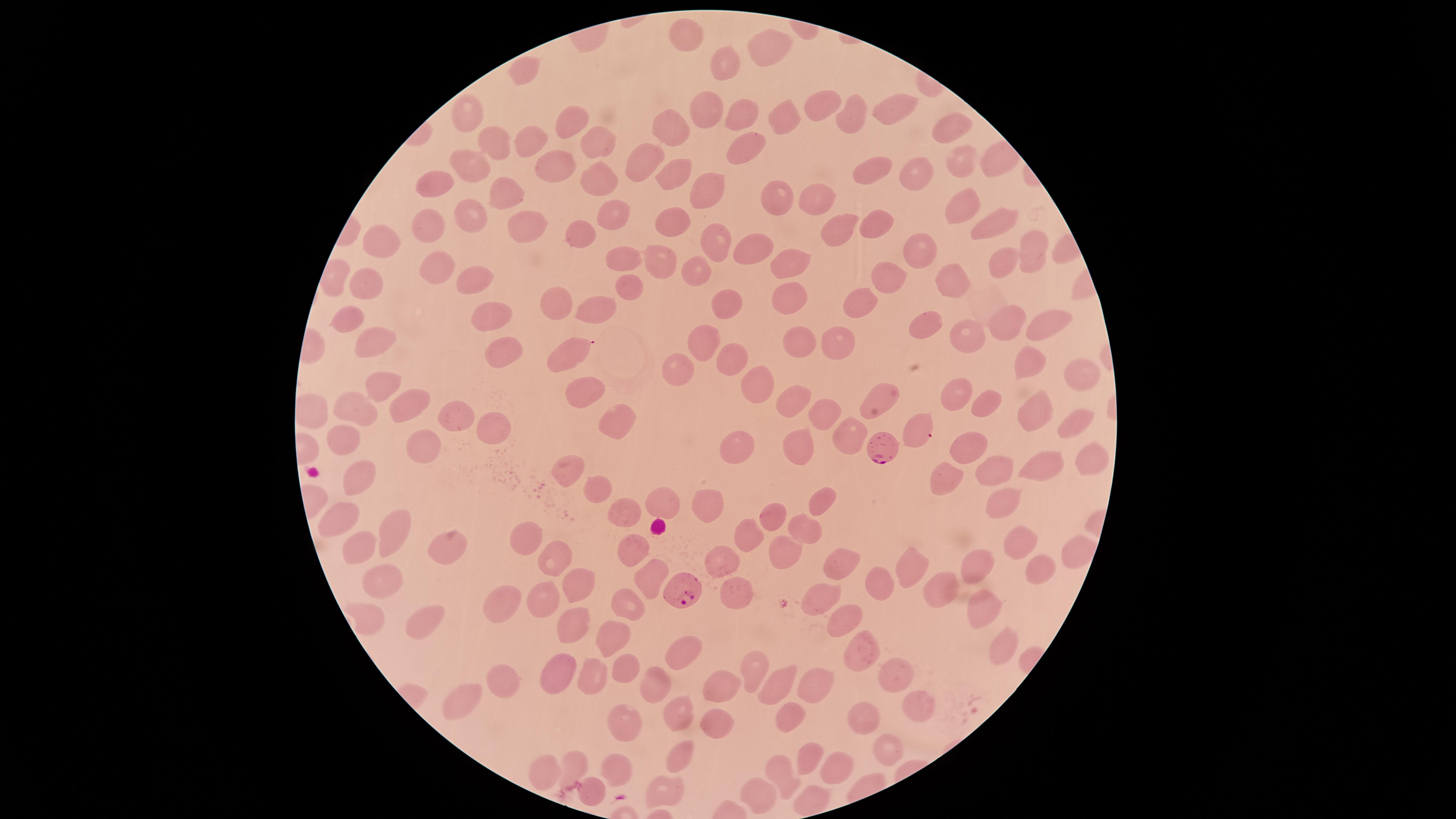
{
  "visible_region": "circular",
  "preparation": "thin blood film",
  "capture": "smartphone photograph through the microscope eyepiece",
  "parasitized_red_blood_cells": "approximate marker points, in pixels from the top-left corner: (x=876, y=453), (x=683, y=595)",
  "species": "Plasmodium falciparum",
  "field_of_view": "single",
  "image_size": "1456×819 pixels",
  "uninfected_red_blood_cells": "approximate marker points, in pixels from the top-left corner: (x=689, y=28), (x=774, y=44), (x=727, y=61), (x=521, y=67), (x=829, y=98), (x=475, y=105), (x=897, y=109), (x=707, y=114), (x=853, y=116), (x=739, y=117), (x=782, y=118), (x=572, y=122), (x=671, y=126), (x=950, y=130), (x=533, y=140), (x=592, y=144), (x=749, y=144), (x=495, y=146), (x=645, y=156), (x=994, y=157), (x=962, y=159), (x=473, y=161), (x=559, y=164), (x=676, y=168), (x=871, y=172), (x=919, y=173), (x=595, y=175), (x=439, y=185), (x=702, y=190), (x=504, y=194), (x=818, y=194), (x=778, y=199), (x=967, y=206), (x=468, y=214), (x=608, y=215), (x=678, y=218), (x=875, y=221), (x=993, y=223), (x=525, y=224), (x=426, y=225), (x=836, y=225), (x=578, y=233), (x=716, y=239), (x=753, y=244), (x=384, y=246), (x=922, y=251), (x=1030, y=252), (x=625, y=258), (x=791, y=258), (x=1001, y=259), (x=658, y=263), (x=698, y=270), (x=439, y=272), (x=889, y=275), (x=475, y=277), (x=955, y=277), (x=369, y=282), (x=632, y=285), (x=785, y=292), (x=555, y=298), (x=725, y=298), (x=599, y=302), (x=859, y=307), (x=494, y=309), (x=1048, y=317), (x=349, y=318), (x=922, y=325), (x=1005, y=325), (x=964, y=337), (x=712, y=338), (x=840, y=339), (x=373, y=342), (x=807, y=342), (x=506, y=347), (x=575, y=352), (x=725, y=354), (x=676, y=363), (x=1030, y=364), (x=1085, y=375), (x=384, y=382), (x=754, y=383), (x=578, y=386), (x=884, y=392), (x=960, y=396), (x=793, y=400), (x=349, y=402), (x=827, y=405), (x=988, y=405), (x=1041, y=405), (x=411, y=407), (x=452, y=411), (x=620, y=411), (x=491, y=422), (x=1074, y=422), (x=914, y=425), (x=855, y=426), (x=345, y=437), (x=799, y=442), (x=974, y=443), (x=736, y=444), (x=420, y=447), (x=1095, y=458), (x=1042, y=462), (x=997, y=466), (x=567, y=473), (x=944, y=474), (x=355, y=479), (x=596, y=496), (x=664, y=497), (x=1001, y=499), (x=821, y=501), (x=705, y=503), (x=630, y=509), (x=767, y=511), (x=335, y=516), (x=803, y=525), (x=395, y=537), (x=527, y=538), (x=1015, y=538), (x=748, y=539), (x=357, y=543), (x=447, y=543), (x=777, y=548), (x=631, y=549), (x=1074, y=552), (x=549, y=553), (x=835, y=560), (x=918, y=561), (x=723, y=563), (x=982, y=563), (x=1043, y=566), (x=646, y=574), (x=388, y=582), (x=573, y=582), (x=944, y=585), (x=877, y=587), (x=733, y=592), (x=506, y=599), (x=823, y=600), (x=548, y=604), (x=627, y=604), (x=975, y=608), (x=421, y=622), (x=569, y=622), (x=840, y=622), (x=615, y=632), (x=997, y=641), (x=860, y=646), (x=687, y=657), (x=751, y=664), (x=619, y=666), (x=897, y=668), (x=554, y=669), (x=593, y=676), (x=501, y=677), (x=769, y=682), (x=819, y=682), (x=653, y=683), (x=723, y=686), (x=464, y=695), (x=920, y=700), (x=680, y=715), (x=789, y=715), (x=865, y=717), (x=712, y=721), (x=632, y=726), (x=893, y=744), (x=682, y=751), (x=811, y=752), (x=574, y=757), (x=832, y=763), (x=613, y=764), (x=539, y=767), (x=784, y=772), (x=661, y=792), (x=758, y=795), (x=590, y=796)",
  "presence": "malaria parasites seen",
  "stain": "Giemsa"
}